Locate every blood parasite and identify its species.
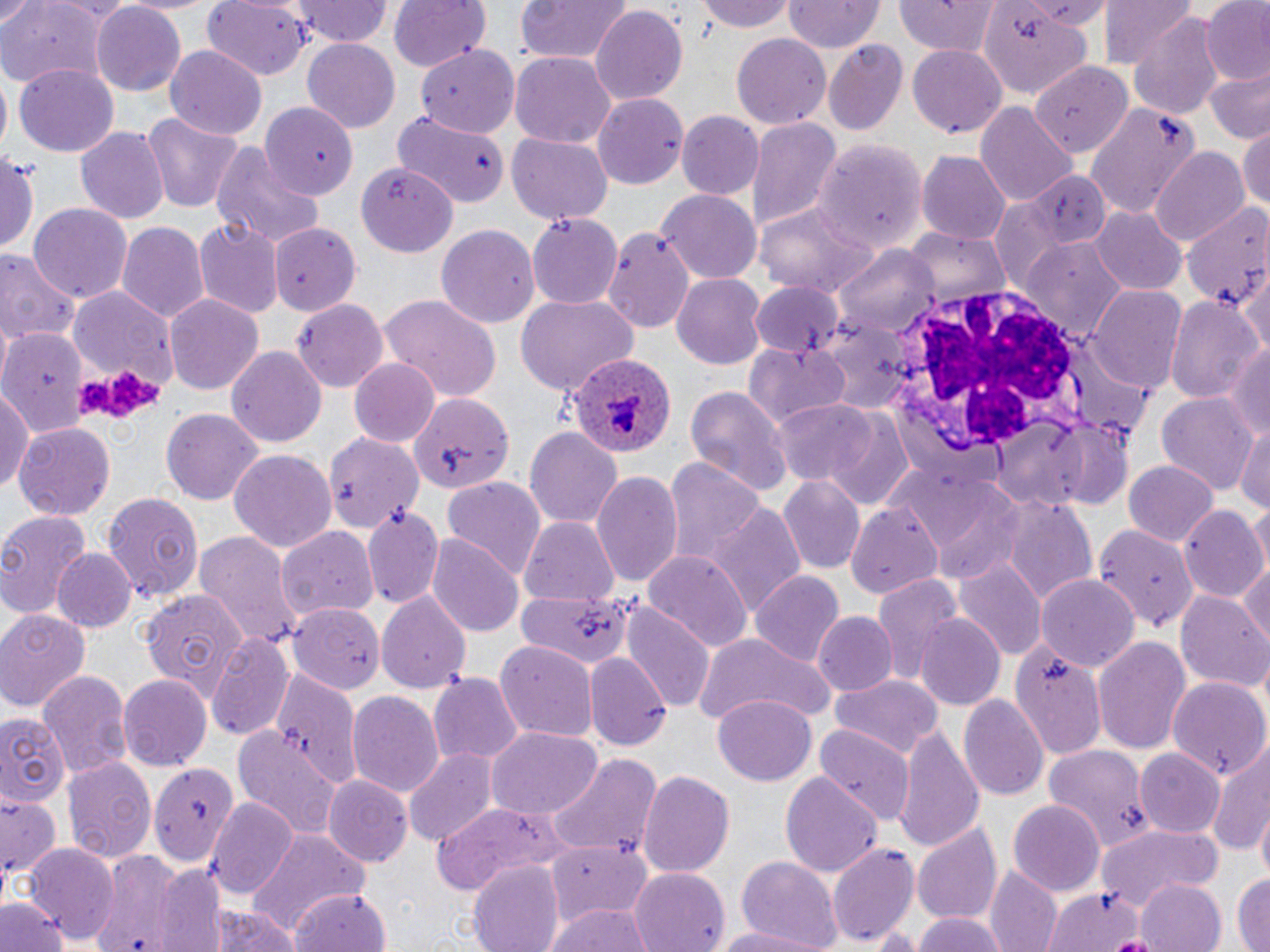

Approximate bounding boxes as named x1/y1/x2/y2 corners in pixels.
Plasmodium ovale-infected red blood cells: (x1=565, y1=355, x2=674, y2=456).
No Plasmodium falciparum, Plasmodium malariae, Plasmodium vivax, Babesia divergens, or Trypanosoma brucei observed.

slide-level diagnosis = Plasmodium ovale
field of view = one of a larger specimen
platelet locations = approximate bounding boxes as named x1/y1/x2/y2 corners in pixels: (x1=75, y1=369, x2=162, y2=421)
white blood cell locations = approximate bounding boxes as named x1/y1/x2/y2 corners in pixels: (x1=887, y1=284, x2=1098, y2=461)
preparation = thin blood smear
image size = 1270×952 pixels
magnification = 1000x
stain = May-Grünwald-Giemsa
uninfected red blood cell locations = approximate bounding boxes as named x1/y1/x2/y2 corners in pixels: (x1=117, y1=0, x2=221, y2=15), (x1=388, y1=0, x2=489, y2=71), (x1=513, y1=0, x2=629, y2=67), (x1=699, y1=0, x2=796, y2=33), (x1=893, y1=0, x2=1003, y2=56), (x1=1101, y1=0, x2=1198, y2=76), (x1=202, y1=1, x2=309, y2=79), (x1=294, y1=1, x2=392, y2=46), (x1=783, y1=1, x2=883, y2=56), (x1=1200, y1=1, x2=1270, y2=87), (x1=90, y1=2, x2=186, y2=94), (x1=0, y1=3, x2=110, y2=89), (x1=981, y1=5, x2=1096, y2=99), (x1=591, y1=6, x2=687, y2=105), (x1=1129, y1=12, x2=1225, y2=120), (x1=731, y1=34, x2=831, y2=129), (x1=301, y1=38, x2=400, y2=134), (x1=823, y1=40, x2=908, y2=137), (x1=416, y1=44, x2=518, y2=135), (x1=909, y1=44, x2=1007, y2=139), (x1=165, y1=45, x2=267, y2=140), (x1=510, y1=52, x2=617, y2=148), (x1=1029, y1=61, x2=1135, y2=152), (x1=14, y1=64, x2=120, y2=158), (x1=1203, y1=68, x2=1270, y2=144), (x1=593, y1=94, x2=688, y2=187), (x1=262, y1=101, x2=357, y2=199), (x1=976, y1=101, x2=1076, y2=209), (x1=1087, y1=102, x2=1202, y2=219), (x1=138, y1=111, x2=248, y2=212), (x1=677, y1=111, x2=765, y2=201), (x1=393, y1=115, x2=508, y2=208), (x1=746, y1=118, x2=840, y2=232), (x1=74, y1=124, x2=168, y2=222), (x1=1238, y1=124, x2=1270, y2=212), (x1=507, y1=133, x2=612, y2=224), (x1=815, y1=138, x2=928, y2=255), (x1=210, y1=144, x2=326, y2=251), (x1=1, y1=148, x2=39, y2=259), (x1=1151, y1=148, x2=1250, y2=247), (x1=917, y1=150, x2=1009, y2=246), (x1=360, y1=162, x2=459, y2=258), (x1=997, y1=168, x2=1112, y2=269), (x1=659, y1=192, x2=759, y2=283), (x1=987, y1=198, x2=1073, y2=295), (x1=1184, y1=198, x2=1270, y2=308), (x1=755, y1=199, x2=875, y2=299), (x1=29, y1=202, x2=132, y2=303), (x1=1091, y1=207, x2=1187, y2=296), (x1=527, y1=211, x2=623, y2=311), (x1=193, y1=219, x2=282, y2=318), (x1=116, y1=220, x2=210, y2=324), (x1=268, y1=221, x2=362, y2=309), (x1=436, y1=225, x2=539, y2=330), (x1=601, y1=225, x2=695, y2=333), (x1=904, y1=230, x2=1010, y2=307), (x1=1023, y1=239, x2=1125, y2=342), (x1=837, y1=243, x2=939, y2=336), (x1=1, y1=252, x2=80, y2=347), (x1=672, y1=273, x2=766, y2=367), (x1=1238, y1=273, x2=1269, y2=358), (x1=751, y1=280, x2=846, y2=358), (x1=1086, y1=286, x2=1187, y2=395), (x1=71, y1=289, x2=178, y2=393), (x1=378, y1=292, x2=502, y2=402), (x1=165, y1=294, x2=264, y2=396), (x1=1166, y1=294, x2=1264, y2=405), (x1=517, y1=295, x2=637, y2=398), (x1=293, y1=298, x2=388, y2=390), (x1=818, y1=315, x2=913, y2=411), (x1=2, y1=327, x2=88, y2=436), (x1=744, y1=340, x2=850, y2=428), (x1=1223, y1=340, x2=1270, y2=446), (x1=227, y1=347, x2=327, y2=446), (x1=348, y1=357, x2=440, y2=447), (x1=0, y1=383, x2=33, y2=498), (x1=685, y1=385, x2=791, y2=500), (x1=1157, y1=390, x2=1260, y2=496), (x1=410, y1=394, x2=515, y2=492), (x1=774, y1=397, x2=883, y2=485), (x1=819, y1=407, x2=916, y2=510), (x1=161, y1=410, x2=263, y2=504), (x1=1234, y1=421, x2=1270, y2=518), (x1=13, y1=422, x2=116, y2=521), (x1=524, y1=426, x2=626, y2=528), (x1=326, y1=435, x2=425, y2=534), (x1=227, y1=450, x2=338, y2=555), (x1=665, y1=456, x2=767, y2=567), (x1=892, y1=459, x2=1027, y2=579), (x1=1122, y1=459, x2=1219, y2=547), (x1=590, y1=471, x2=682, y2=589), (x1=441, y1=476, x2=547, y2=580), (x1=776, y1=477, x2=863, y2=572), (x1=103, y1=493, x2=204, y2=606), (x1=998, y1=493, x2=1098, y2=608), (x1=1251, y1=498, x2=1270, y2=581), (x1=845, y1=501, x2=943, y2=601), (x1=706, y1=504, x2=807, y2=621), (x1=362, y1=505, x2=445, y2=610), (x1=1177, y1=505, x2=1267, y2=602), (x1=0, y1=511, x2=93, y2=616), (x1=517, y1=515, x2=620, y2=607), (x1=276, y1=523, x2=381, y2=626), (x1=1093, y1=523, x2=1196, y2=632), (x1=193, y1=531, x2=301, y2=651), (x1=426, y1=533, x2=522, y2=635), (x1=641, y1=546, x2=754, y2=652), (x1=50, y1=548, x2=135, y2=632), (x1=1239, y1=558, x2=1270, y2=651), (x1=955, y1=561, x2=1046, y2=661), (x1=752, y1=572, x2=843, y2=668), (x1=869, y1=574, x2=965, y2=686), (x1=1037, y1=574, x2=1139, y2=671), (x1=137, y1=586, x2=252, y2=700), (x1=516, y1=590, x2=630, y2=669), (x1=378, y1=591, x2=471, y2=693), (x1=1176, y1=591, x2=1270, y2=691), (x1=285, y1=604, x2=385, y2=688), (x1=623, y1=604, x2=715, y2=710), (x1=0, y1=609, x2=89, y2=712), (x1=814, y1=613, x2=897, y2=697), (x1=915, y1=615, x2=1006, y2=712), (x1=204, y1=631, x2=293, y2=742), (x1=691, y1=633, x2=834, y2=726), (x1=1092, y1=636, x2=1193, y2=759), (x1=493, y1=639, x2=598, y2=741), (x1=1012, y1=644, x2=1108, y2=761), (x1=583, y1=651, x2=671, y2=751), (x1=269, y1=667, x2=361, y2=787), (x1=38, y1=669, x2=133, y2=780), (x1=430, y1=672, x2=526, y2=764), (x1=830, y1=673, x2=943, y2=762), (x1=120, y1=675, x2=211, y2=772), (x1=1167, y1=676, x2=1270, y2=781), (x1=345, y1=690, x2=444, y2=798), (x1=959, y1=694, x2=1048, y2=801), (x1=712, y1=695, x2=818, y2=787), (x1=0, y1=711, x2=69, y2=806), (x1=232, y1=724, x2=343, y2=843), (x1=817, y1=724, x2=913, y2=822), (x1=892, y1=724, x2=986, y2=851), (x1=486, y1=729, x2=601, y2=822), (x1=1207, y1=738, x2=1270, y2=862), (x1=1043, y1=745, x2=1154, y2=852), (x1=1136, y1=746, x2=1227, y2=837), (x1=404, y1=748, x2=498, y2=846), (x1=545, y1=751, x2=662, y2=863), (x1=64, y1=755, x2=156, y2=861), (x1=150, y1=760, x2=239, y2=865), (x1=637, y1=767, x2=736, y2=878), (x1=780, y1=772, x2=881, y2=878), (x1=324, y1=776, x2=413, y2=866), (x1=0, y1=792, x2=60, y2=884), (x1=205, y1=798, x2=300, y2=900), (x1=1009, y1=799, x2=1104, y2=895), (x1=430, y1=800, x2=566, y2=892), (x1=1255, y1=812, x2=1269, y2=884), (x1=914, y1=822, x2=1002, y2=924), (x1=1097, y1=823, x2=1224, y2=907), (x1=247, y1=830, x2=370, y2=940), (x1=548, y1=839, x2=652, y2=928), (x1=25, y1=840, x2=117, y2=944), (x1=829, y1=842, x2=918, y2=946), (x1=91, y1=848, x2=202, y2=952), (x1=736, y1=856, x2=842, y2=950), (x1=148, y1=859, x2=229, y2=947), (x1=468, y1=860, x2=565, y2=952), (x1=985, y1=864, x2=1062, y2=952), (x1=629, y1=868, x2=730, y2=952), (x1=1232, y1=871, x2=1269, y2=952), (x1=1136, y1=879, x2=1227, y2=952), (x1=286, y1=887, x2=393, y2=952), (x1=1043, y1=887, x2=1148, y2=951), (x1=2, y1=895, x2=67, y2=952), (x1=547, y1=904, x2=657, y2=952), (x1=207, y1=905, x2=304, y2=952), (x1=911, y1=911, x2=1010, y2=952), (x1=712, y1=924, x2=832, y2=952)
modality = light microscopy